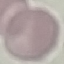

{
  "result": "no malaria parasites seen",
  "capture": "smartphone through the microscope eyepiece",
  "preparation": "thin smear",
  "image_type": "automatically extracted cell patch, resized to 64 × 64 pixels",
  "stain": "Giemsa"
}